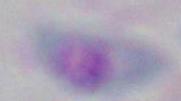 Toxoplasma gondii is seen. Captured at 1000x magnification. Micrograph.